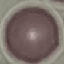
malaria_status: uninfected
capture: smartphone through the microscope eyepiece
image_type: cell patch, automatically extracted from a larger field of view and resized to 64 × 64 pixels
stain: Giemsa
preparation: thin blood film